Assess this cell for malaria.
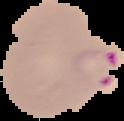

It is parasitized.

Summary:
  - Preparation: thin blood film
  - Image size: 124×121 pixels
  - Image type: segmented cell region with the area outside set to black